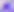

identification = Toxoplasma gondii
modality = micrograph
magnification = 400x